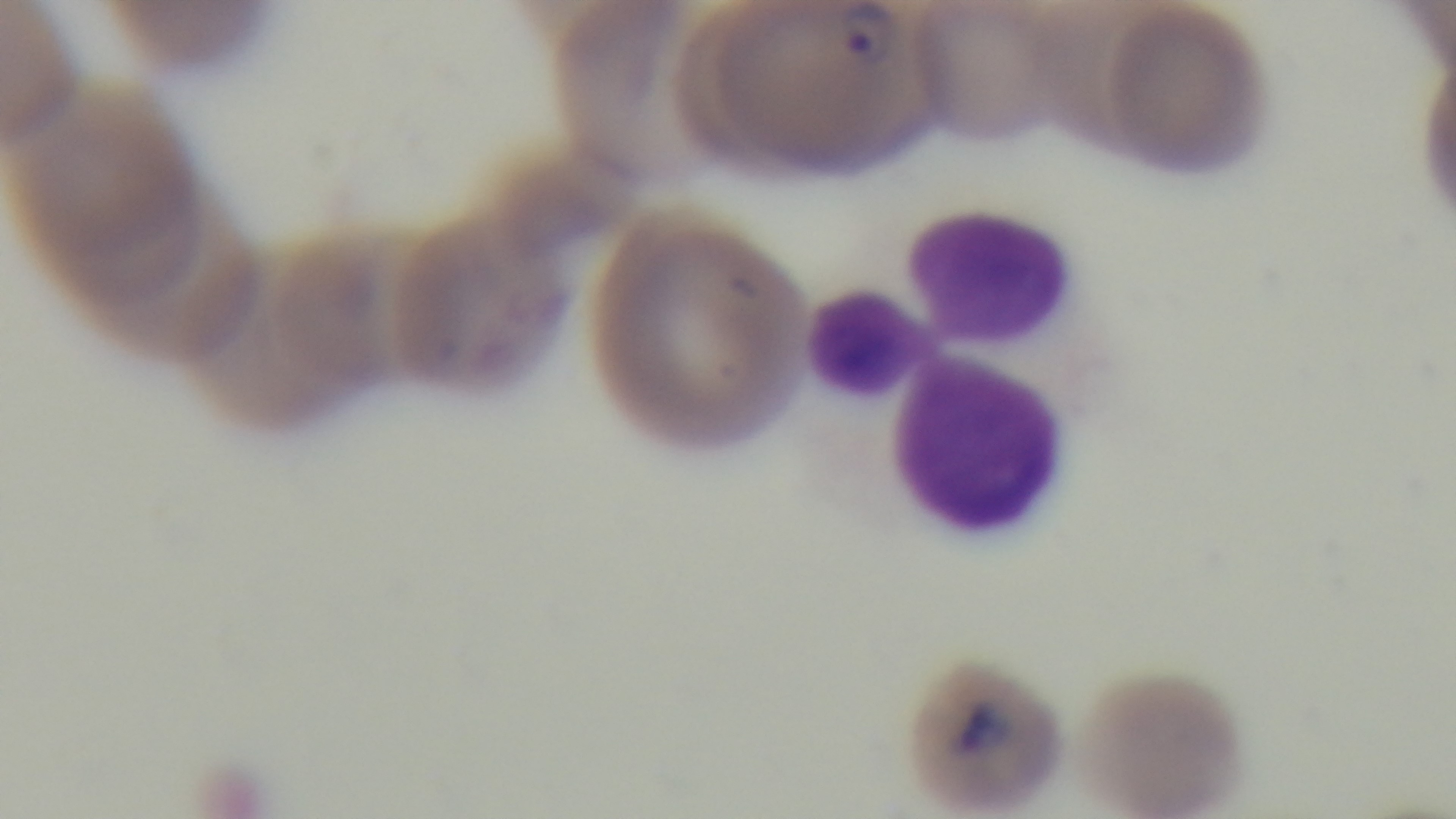 Giemsa stain. Preparation: thin. Malaria status: positive. Oil-immersion objective, 100x. Light microscopy. Captured with a mounted 4K digital camera. Single field of view.